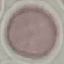
Result: no malaria parasites seen. Automatically extracted cell patch, resized to 64 × 64 pixels. Giemsa-stained preparation. Photographed with a smartphone camera at the microscope eyepiece. Thin smear of blood.